Locate and identify every blood parasite.
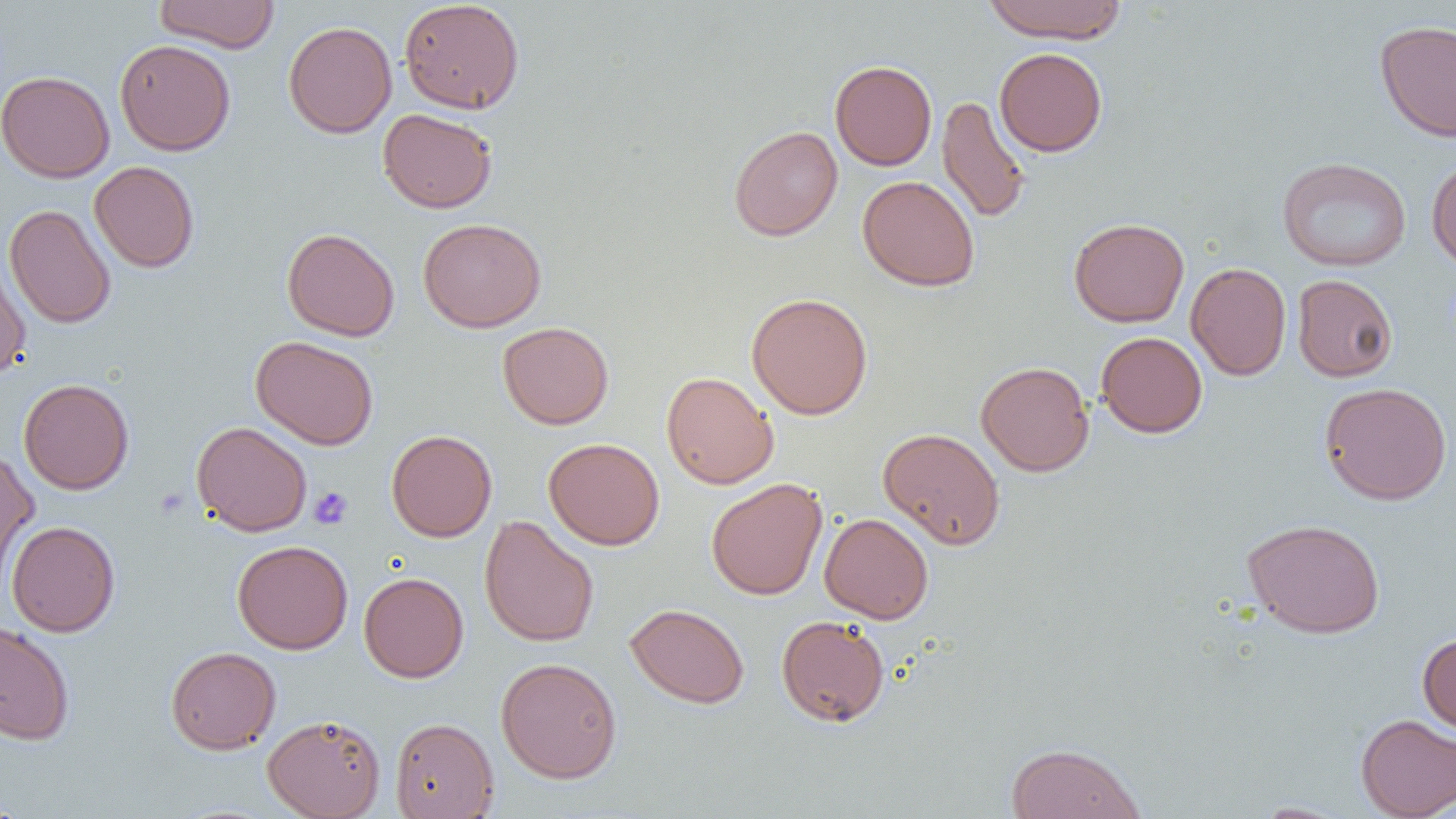

No blood parasites observed.

Approximate bounding boxes as [x1, y1, x2, y2] in pixels. Uninfected red blood cell locations: [154, 0, 280, 52], [399, 0, 525, 114], [982, 0, 1128, 43], [1375, 19, 1456, 142], [283, 21, 397, 138], [115, 40, 236, 155], [994, 47, 1107, 157], [830, 60, 937, 170], [0, 69, 115, 182], [937, 95, 1031, 223], [378, 108, 497, 213], [729, 125, 843, 241], [1277, 156, 1411, 271], [1426, 156, 1456, 269], [89, 161, 200, 273], [857, 175, 980, 291], [4, 204, 116, 329], [418, 217, 547, 332], [1069, 217, 1189, 327], [282, 227, 400, 341], [0, 255, 31, 383], [1186, 262, 1292, 381], [1292, 274, 1398, 382], [746, 292, 873, 419], [497, 322, 614, 429], [1095, 331, 1208, 438], [250, 335, 379, 450], [975, 361, 1094, 476], [661, 371, 778, 489], [19, 378, 134, 494], [1319, 382, 1452, 506], [191, 421, 312, 536], [878, 427, 1005, 549], [386, 429, 497, 542], [543, 437, 665, 550], [0, 449, 39, 586], [706, 478, 827, 600], [819, 512, 934, 624], [479, 515, 599, 647], [1242, 517, 1385, 638], [6, 521, 120, 636], [232, 539, 353, 654], [359, 572, 469, 682], [625, 603, 750, 708], [776, 616, 889, 727], [0, 622, 75, 744], [1417, 632, 1456, 734], [165, 646, 281, 754], [495, 657, 623, 783], [262, 714, 385, 819], [1356, 714, 1456, 818], [390, 717, 499, 819], [1005, 742, 1146, 818], [1251, 801, 1355, 818]. Platelet locations: [309, 486, 353, 530]. Slide-level diagnosis: negative for blood parasites. One field of a larger specimen. Optical microscopy. Image is 1456×819 pixels. Captured at 1000x magnification. Thin blood film.